Assess this cell for malaria.
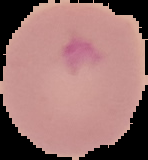
It is parasitized.

Image is 148×160 pixels. From a thin blood film. Cell region segmented out of the field of view; the surrounding area is masked to black.